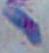

modality = photomicrograph
magnification = 1000x
identification = Toxoplasma gondii